Locate every blood parasite and identify its species.
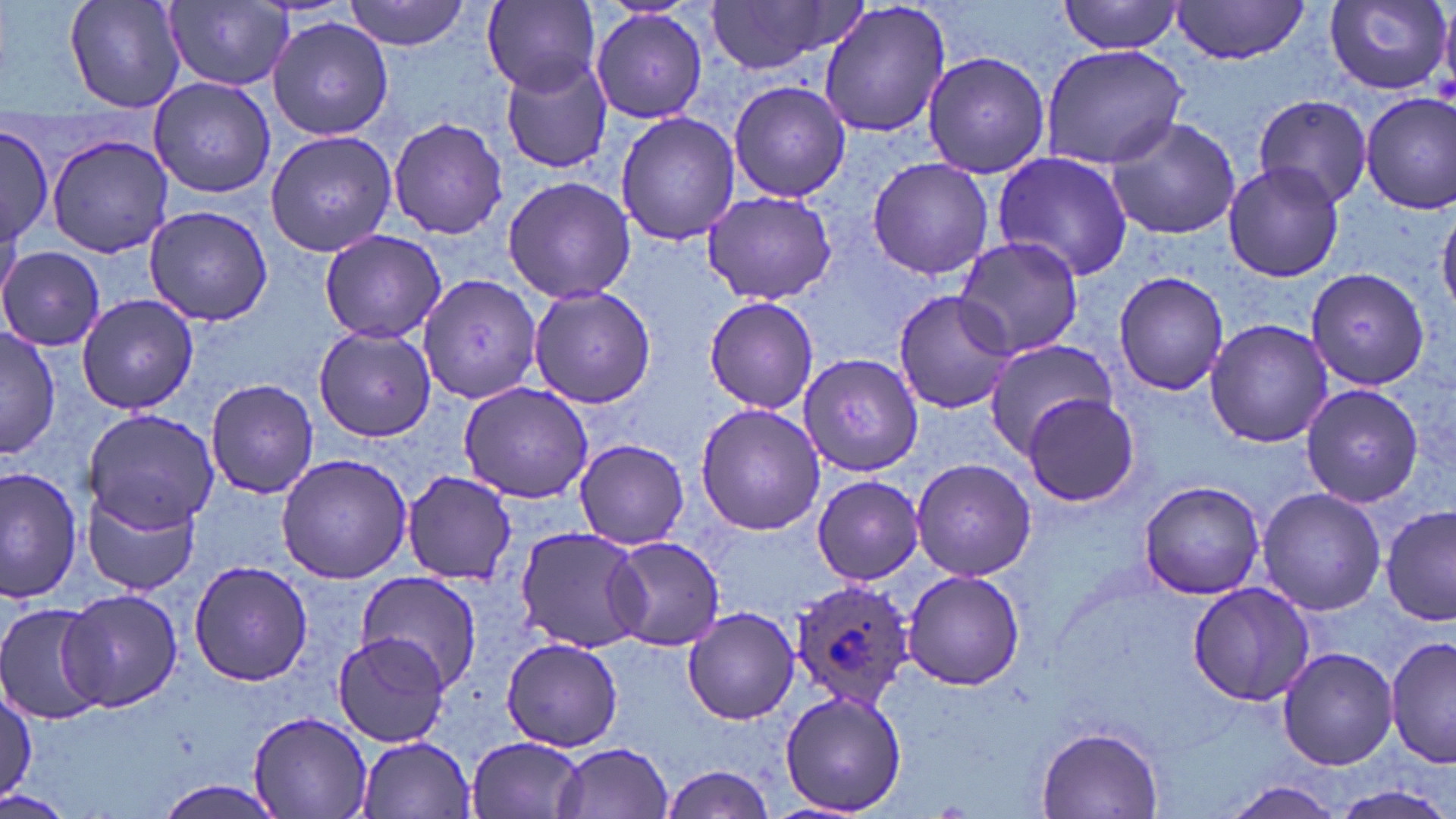

Approximate bounding boxes as (x1,y1)-(x2,y2) corner pairs in pixels.
Plasmodium ovale-infected red blood cells: (789,580)-(916,711).
No Plasmodium falciparum, Plasmodium malariae, Plasmodium vivax, Babesia divergens, or Trypanosoma brucei observed.

slide-level diagnosis = Plasmodium ovale
magnification = 1000x
field of view = one of a larger specimen
modality = optical microscopy
stain = May-Grünwald-Giemsa
preparation = thin blood smear
image size = 1456×819 pixels
uninfected red blood cell locations = approximate bounding boxes as (x1,y1)-(x2,y2) corner pairs in pixels: (63,0)-(184,113), (343,0)-(474,51), (706,0)-(860,77), (1058,0)-(1185,55), (1327,0)-(1454,95), (164,1)-(295,89), (480,1)-(602,97), (818,2)-(953,140), (1169,2)-(1313,65), (589,8)-(708,124), (267,17)-(395,139), (1040,44)-(1188,170), (502,52)-(616,177), (922,52)-(1052,181), (147,76)-(276,199), (726,79)-(851,205), (1252,93)-(1373,208), (1361,93)-(1456,214), (614,110)-(741,247), (1104,115)-(1243,241), (388,117)-(509,239), (0,122)-(54,253), (265,129)-(397,257), (46,133)-(176,258), (992,151)-(1136,283), (865,157)-(993,280), (1222,161)-(1346,283), (502,175)-(635,305), (701,190)-(837,305), (143,205)-(273,326), (1437,206)-(1456,314), (319,229)-(445,344), (951,235)-(1086,358), (0,246)-(104,350), (1305,266)-(1432,392), (1113,269)-(1230,395), (421,274)-(542,407), (527,283)-(658,408), (892,290)-(1018,414), (75,292)-(196,416), (704,294)-(818,415), (1204,319)-(1332,448), (1,326)-(60,457), (314,326)-(439,441), (982,337)-(1118,456), (799,354)-(923,477), (205,377)-(319,498), (458,381)-(594,503), (1299,382)-(1425,508), (1023,393)-(1141,507), (694,403)-(825,536), (83,406)-(222,535), (573,439)-(690,549), (276,454)-(411,583), (911,459)-(1036,581), (2,466)-(83,603), (402,471)-(517,586), (812,475)-(923,586), (1140,481)-(1265,600), (82,487)-(198,596), (1256,487)-(1387,615), (1381,504)-(1455,630), (514,526)-(649,652), (607,535)-(726,651), (188,560)-(313,685), (902,571)-(1025,690), (354,572)-(481,694), (1187,581)-(1317,707), (47,588)-(186,719), (0,603)-(113,725), (682,606)-(801,724), (333,632)-(452,747), (1385,634)-(1455,770), (501,636)-(624,751), (1277,647)-(1397,770), (0,685)-(35,804), (778,689)-(908,816), (247,711)-(374,819), (1034,724)-(1166,817), (356,735)-(476,819), (465,736)-(589,819), (553,742)-(675,819), (658,764)-(773,819), (154,780)-(289,819), (1219,780)-(1349,818), (1334,784)-(1454,818)